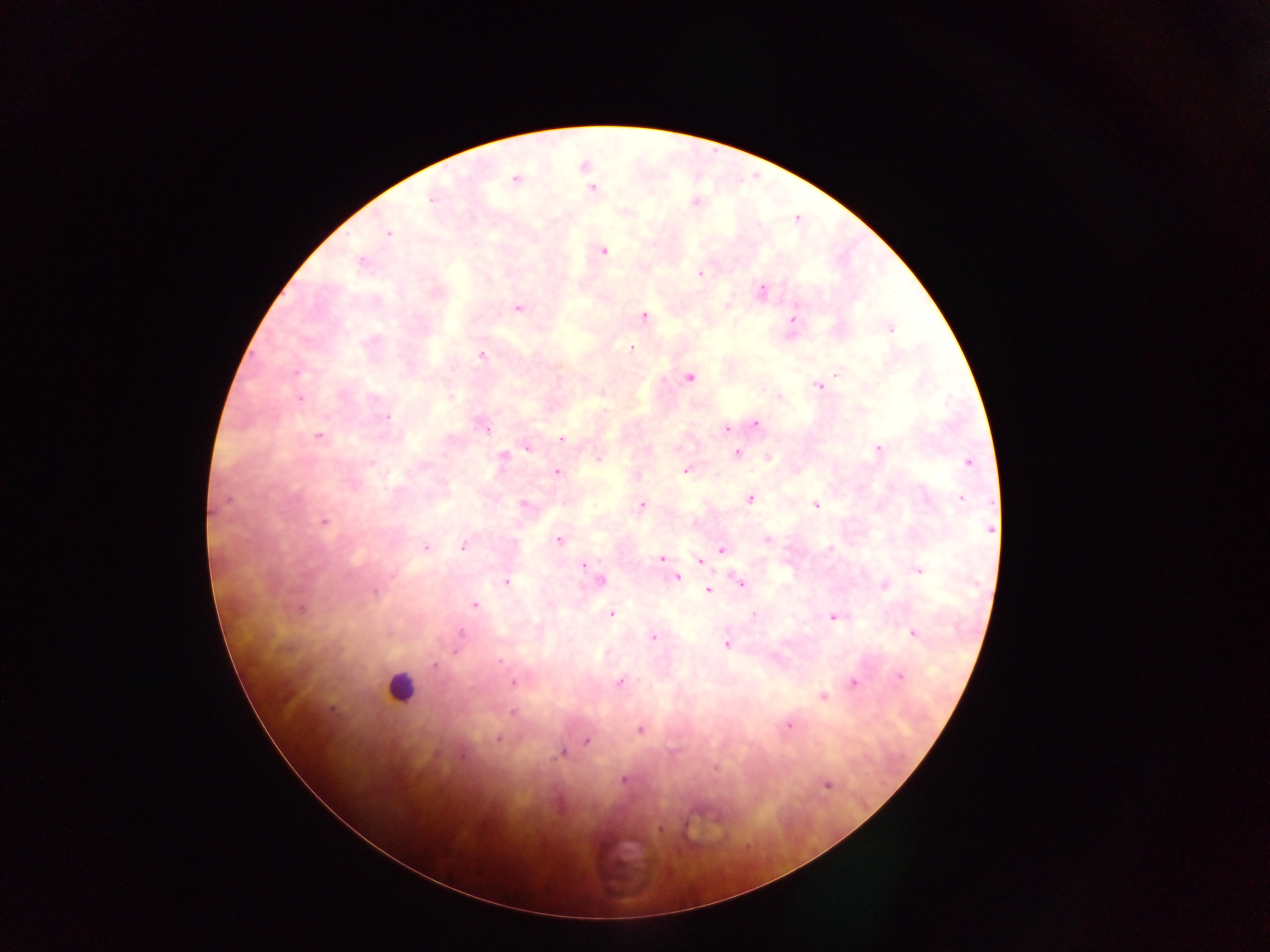

Approximate centers as x y in pixels.
Summary:
  - Malaria parasite locations: 583 166; 515 179; 591 189; 431 198; 387 234; 602 250; 361 261; 700 274; 760 291; 727 306; 518 307; 643 316; 791 321; 889 328; 631 347; 482 355; 837 374; 688 377; 819 385; 299 398; 754 423; 483 424; 726 428; 318 436; 561 439; 526 446; 878 449; 735 454; 767 456; 502 457; 968 463; 686 469; 557 472; 749 497; 961 498; 523 503; 815 504; 641 505; 323 521; 766 539; 559 540; 463 545; 425 547; 721 549; 662 558; 666 560; 699 560; 582 566; 918 569; 677 577; 505 581; 599 581; 741 582; 884 584; 708 590; 475 605; 610 613; 832 617; 912 632; 653 637; 726 644; 456 650; 433 665; 899 677; 620 681; 513 682; 853 683; 822 695; 512 711; 787 724; 639 730; 497 739; 587 741; 563 752; 826 784
  - Leukocyte locations: 399 687
  - Image size: 1270×952 pixels
  - Country: Ghana
  - Preparation: thick blood film
  - Field of view: single
  - Capture: mobile-phone photograph through a microscope